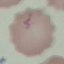

Malaria status: uninfected. Thin blood film. Cell patch, automatically extracted from a larger field of view and resized to 64 × 64 pixels. Giemsa-stained preparation. Acquired by smartphone through the microscope eyepiece.